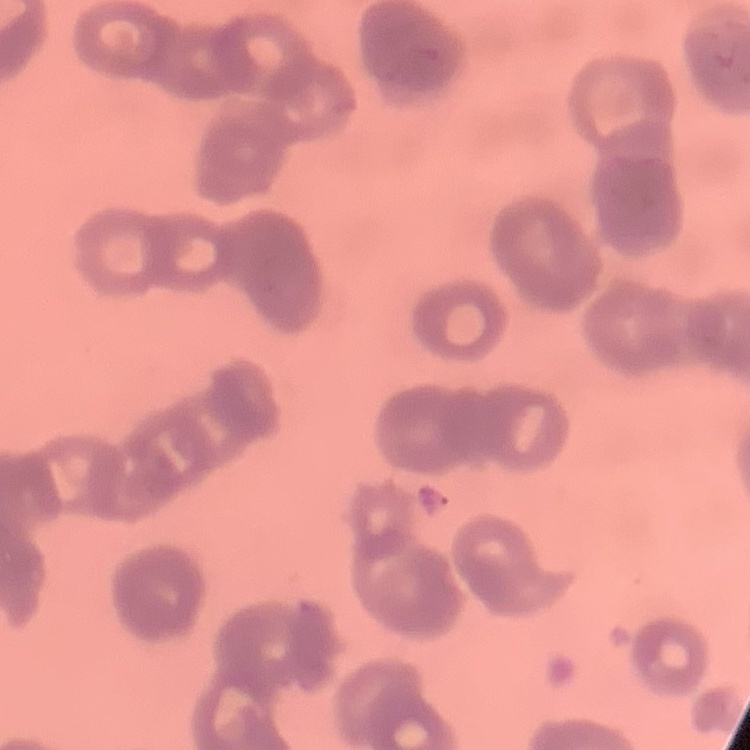
The erythrocytes exhibit rouleaux formation. Stained with either Field's or Giemsa. Thin blood smear. One tile cut from a larger photomicrograph.